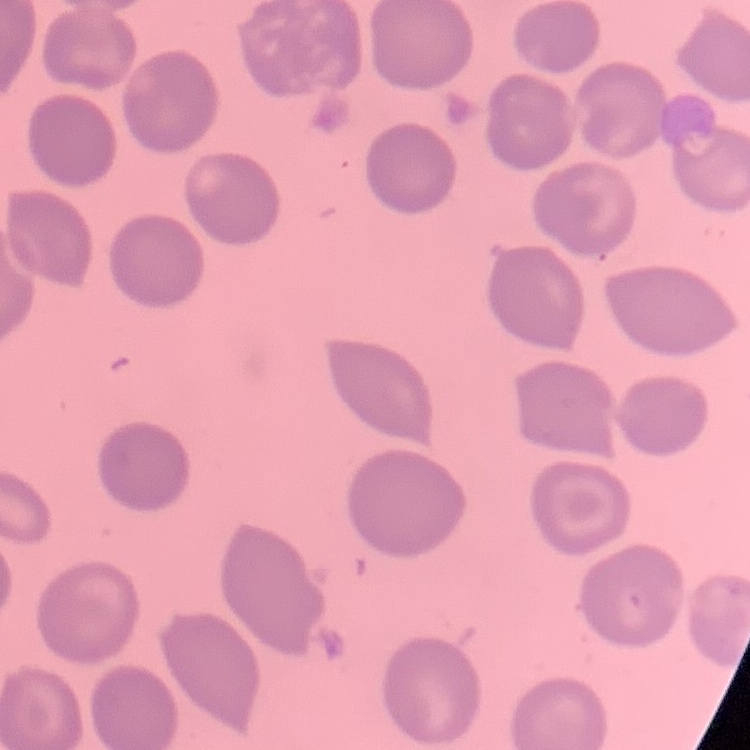
The erythrocytes show no rouleaux formation. Field's or Giemsa stain. One tile cut from a larger photomicrograph. Thin blood film.